Report the malaria status of this cell.
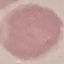
Uninfected.

Giemsa-stained preparation. Thin smear of blood. Cell patch, automatically extracted from a larger field of view and resized to 64 × 64 pixels. Photographed with a smartphone camera at the microscope eyepiece.